Comment on the morphology of the erythrocytes.
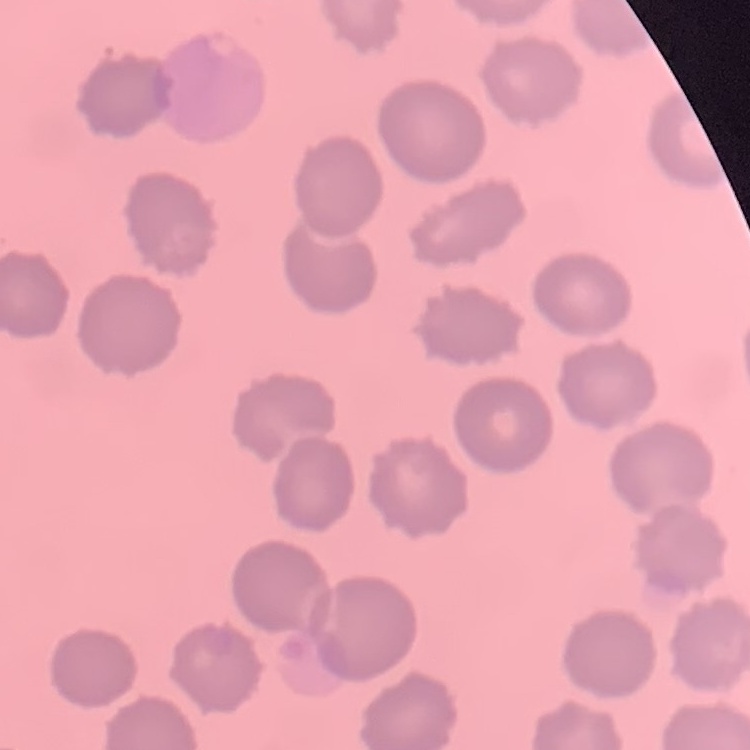
No rouleaux formation.

Summary:
  - Preparation: thin peripheral smear
  - Image type: square crop of a larger photomicrograph
  - Stain: Field's or Giemsa